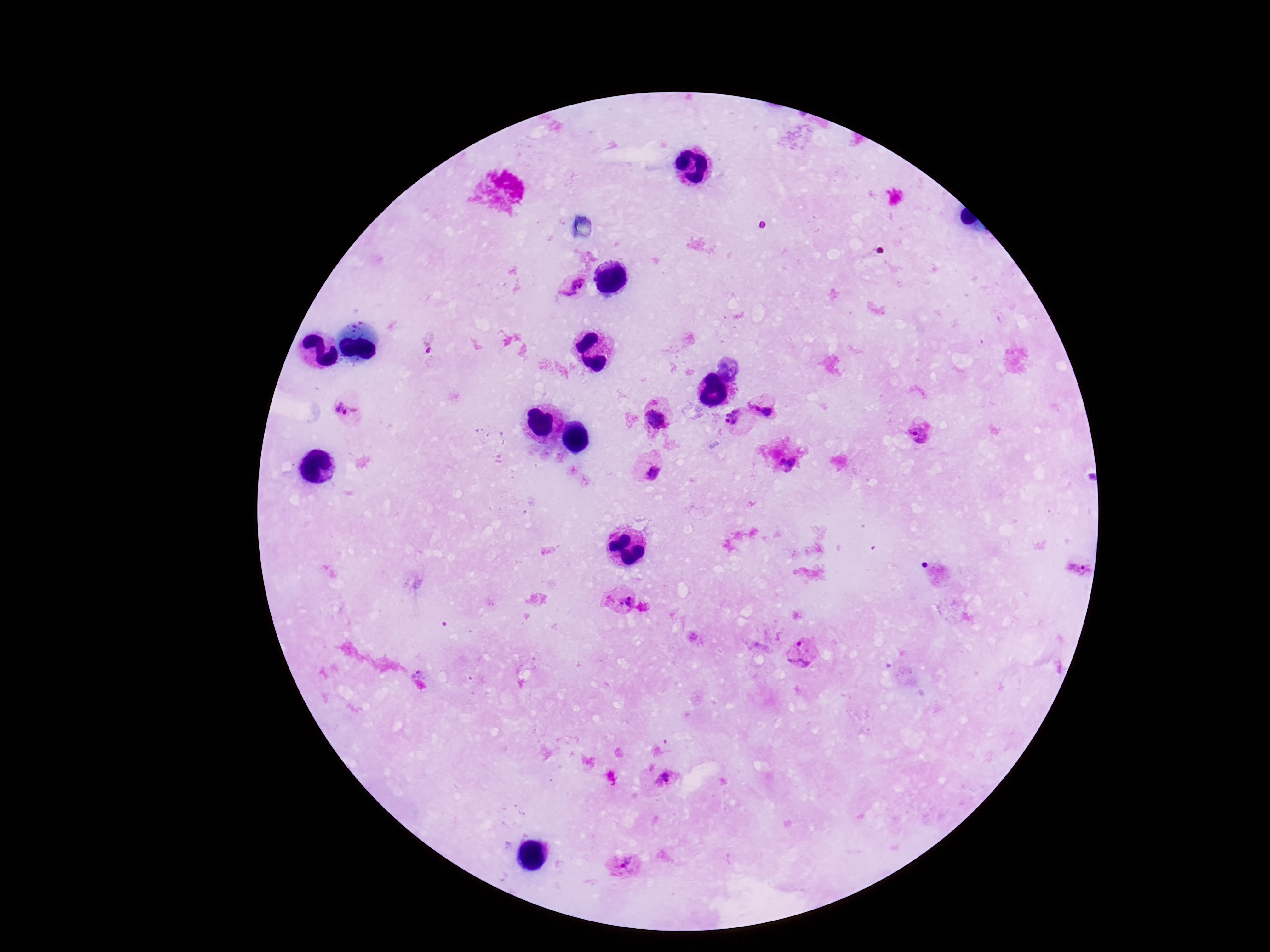
Approximate centers as (x, y) in pixels.
Summary:
  - Plasmodium parasite locations: (575, 287), (431, 343), (731, 369), (766, 403), (347, 412), (656, 419), (739, 421), (919, 430), (650, 467), (621, 601), (804, 656), (667, 786), (625, 868)
  - Magnification: 100x
  - Patient malaria status: infected
  - Preparation: thick blood film
  - Image size: 1270×952 pixels
  - Capture: smartphone camera through the microscope eyepiece
  - Stain: Giemsa
  - Field of view: single